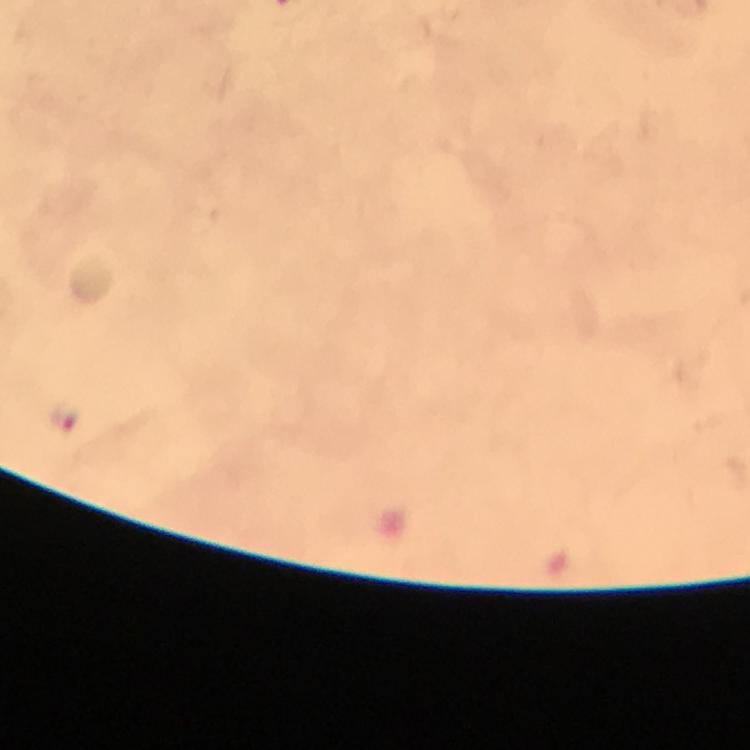
Approximate centers as (x, y) in pixels. Plasmodium parasite locations: (64, 420). Giemsa stain. At 100x magnification. Smartphone photograph taken through a microscope. Immersion oil applied. A crop from one field of view. Image is 750×750 pixels. Thick blood smear. From a malaria diagnostic workup.